State which parasite is depicted.
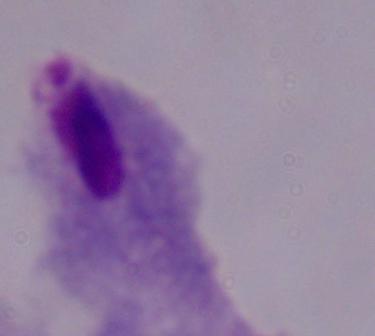
This is a trichomonad.

Summary:
  - Modality: photomicrograph
  - Magnification: 1000x